Name the blood parasite species.
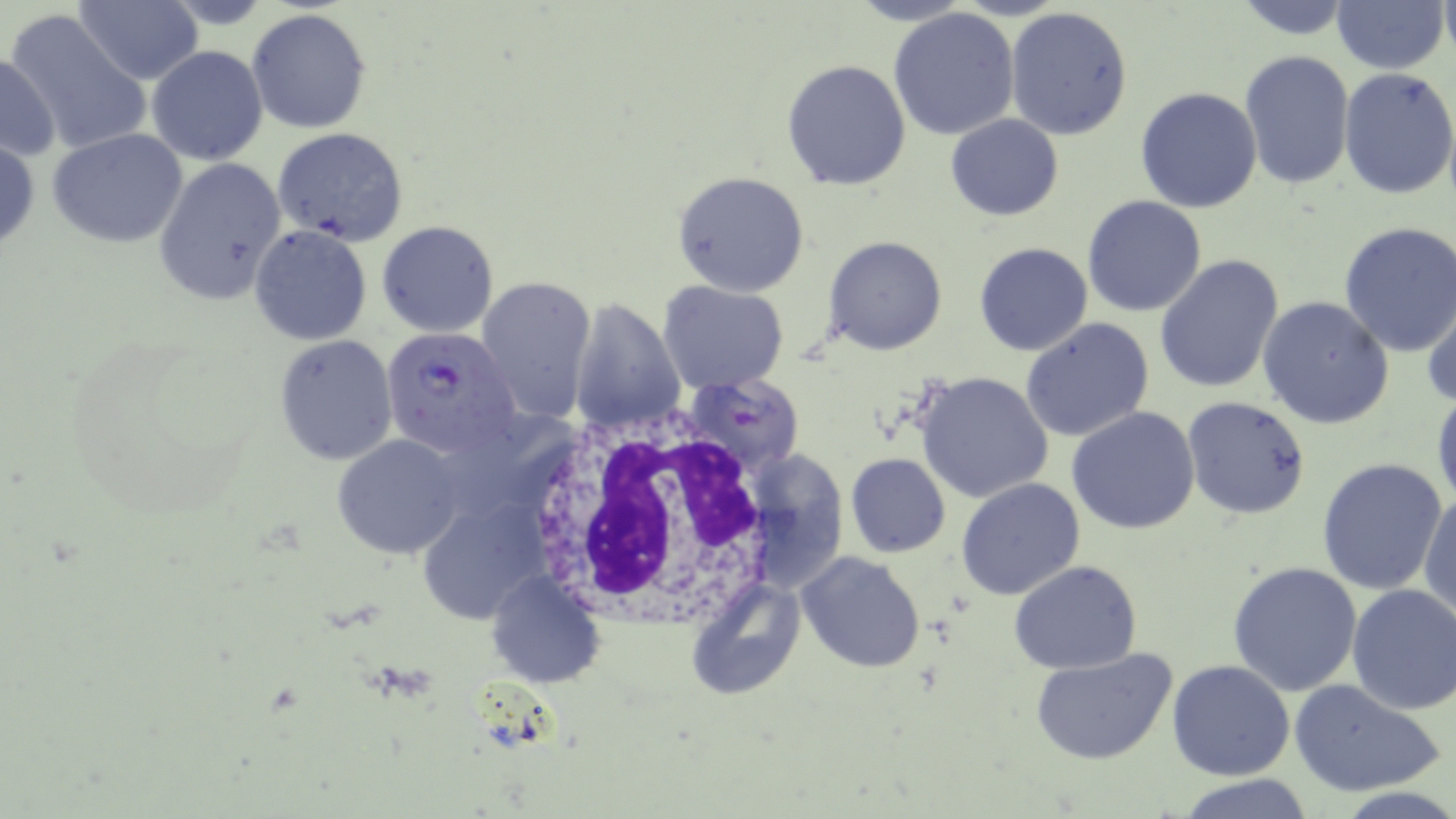

Plasmodium falciparum.

Summary:
  - Coordinate format: approximate bounding boxes as (x1,y1)-(x2,y2) corner pairs in pixels
  - Uninfected red blood cell locations: (73,0)-(203,85), (1228,0)-(1359,39), (1333,1)-(1448,75), (1005,6)-(1133,142), (247,8)-(373,134), (888,8)-(1021,141), (3,10)-(152,157), (147,45)-(267,164), (0,51)-(60,162), (1238,51)-(1355,190), (781,59)-(911,190), (1339,67)-(1456,201), (1134,87)-(1263,214), (945,114)-(1063,221), (271,127)-(410,245), (47,128)-(189,247), (0,134)-(41,256), (155,157)-(286,305), (672,170)-(810,296), (1083,195)-(1206,317), (376,219)-(499,337), (1337,223)-(1456,358), (249,225)-(372,346), (824,236)-(946,355), (974,243)-(1093,356), (1155,254)-(1285,395), (476,276)-(595,420), (658,281)-(789,393), (1421,290)-(1456,410), (1258,296)-(1393,430), (569,299)-(686,431), (1020,318)-(1154,442), (274,336)-(398,465), (915,371)-(1056,505), (682,374)-(805,480), (1433,387)-(1456,512), (1181,395)-(1312,520), (1067,407)-(1200,534), (333,435)-(463,559), (737,447)-(848,592), (845,453)-(950,558), (1316,458)-(1448,596), (955,477)-(1086,600), (1418,486)-(1456,624), (415,501)-(540,629), (797,552)-(926,675), (1010,561)-(1142,674), (1228,562)-(1362,696), (486,570)-(609,689), (688,577)-(806,700), (1346,583)-(1456,714), (1030,648)-(1177,767), (1167,660)-(1295,780), (1287,678)-(1445,798), (1176,774)-(1319,818)
  - Plasmodium falciparum-infected red blood cell locations: (380,327)-(522,456)
  - White blood cell locations: (515,409)-(784,621)
  - Stain: May-Grünwald-Giemsa
  - Modality: optical microscopy
  - Field of view: single
  - Preparation: thin blood smear
  - Image size: 1456×819 pixels
  - Magnification: 1000x